Locate platelets.
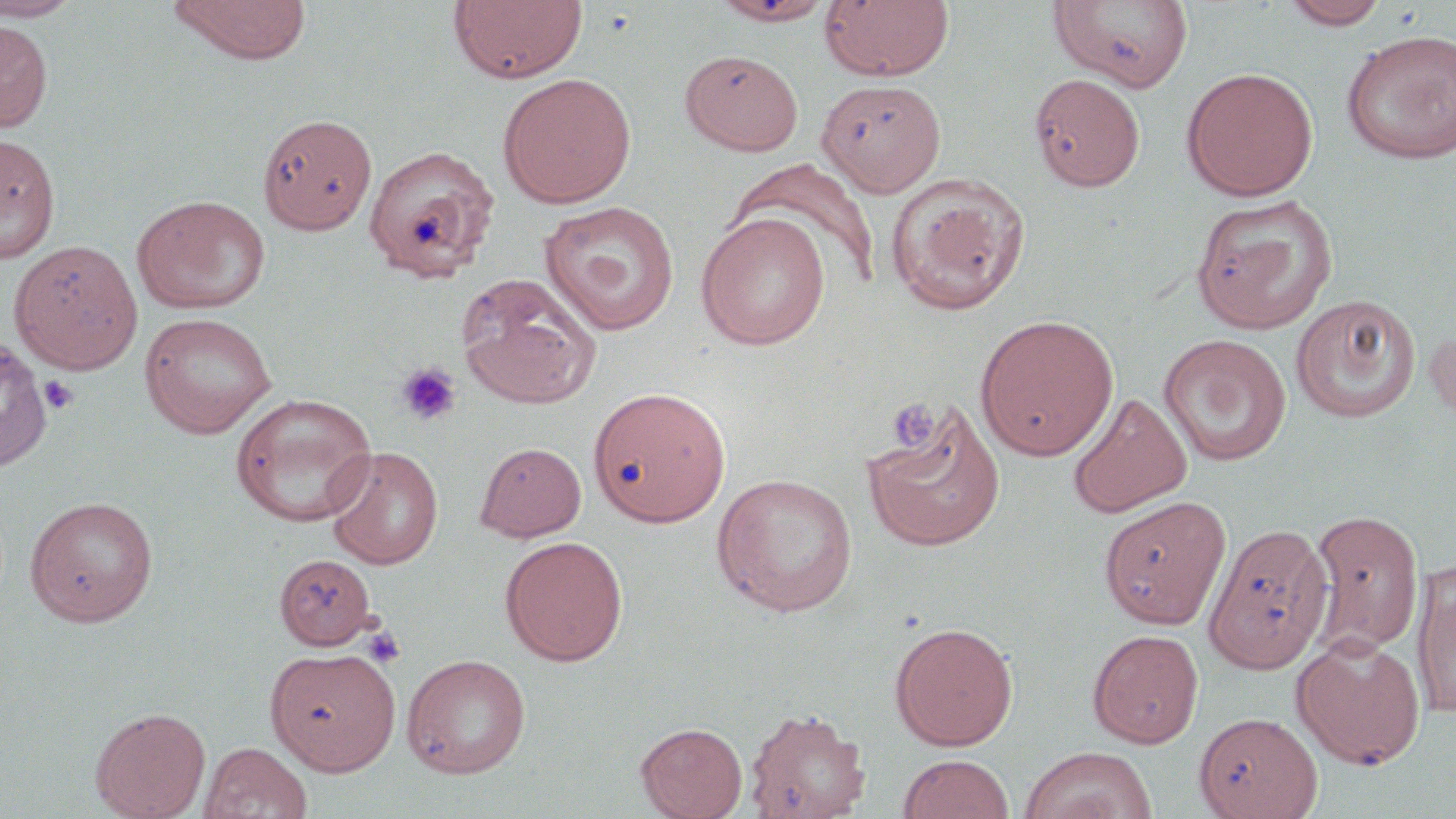

Approximate bounding boxes as (x1, y1, x2, y2) in pixels.
Platelets: (395, 362, 462, 426), (39, 375, 79, 416), (887, 398, 938, 452), (362, 627, 406, 668).

Summary:
  - Uninfected red blood cell locations: (0, 0, 85, 21), (168, 0, 312, 63), (448, 0, 588, 84), (709, 0, 837, 26), (819, 0, 955, 82), (1049, 0, 1195, 92), (1280, 0, 1390, 29), (0, 19, 53, 133), (1340, 29, 1456, 164), (680, 49, 803, 155), (1181, 66, 1319, 201), (497, 72, 637, 208), (1028, 73, 1145, 191), (816, 79, 947, 196), (257, 113, 378, 235), (0, 132, 60, 263), (361, 143, 500, 282), (729, 159, 882, 290), (885, 173, 1031, 316), (131, 194, 270, 315), (1190, 194, 1339, 334), (539, 201, 679, 336), (695, 212, 831, 350), (9, 240, 143, 374), (456, 273, 602, 409), (1291, 294, 1421, 423), (139, 312, 277, 437), (975, 314, 1119, 461), (1424, 324, 1456, 429), (1159, 333, 1292, 466), (0, 337, 53, 472), (588, 386, 731, 528), (1067, 391, 1191, 518), (231, 392, 377, 527), (860, 400, 1006, 553), (475, 441, 587, 542), (323, 445, 444, 570), (711, 473, 859, 617), (24, 495, 159, 626), (1098, 495, 1231, 629), (1307, 507, 1425, 657), (1201, 526, 1331, 679), (499, 535, 629, 666), (274, 553, 378, 650), (1412, 560, 1456, 721), (889, 622, 1019, 750), (1087, 629, 1204, 748), (1292, 634, 1426, 769), (265, 647, 400, 774), (403, 653, 531, 778), (743, 706, 871, 819), (90, 707, 210, 819), (1195, 712, 1322, 819), (635, 721, 747, 818), (199, 741, 313, 819), (1019, 746, 1157, 819), (897, 754, 1015, 819)
  - Slide-level diagnosis: negative for blood parasites
  - Magnification: 1000x
  - Preparation: thin blood smear
  - Field of view: single
  - Stain: May-Grünwald-Giemsa
  - Modality: light microscopy
  - Image size: 1456×819 pixels